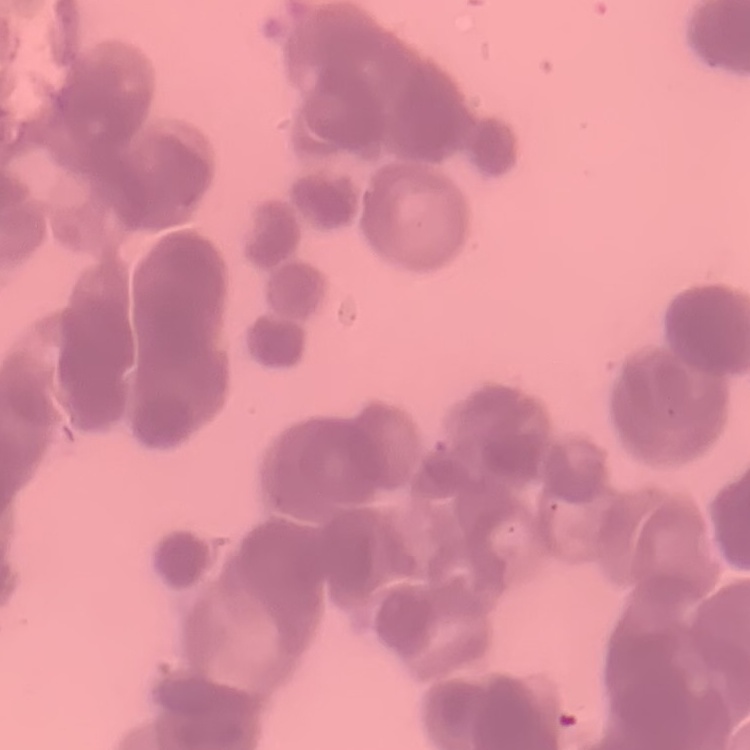
The erythrocytes show rouleaux formation. Square crop of a larger photomicrograph. Field's or Giemsa stain. Thin blood film.